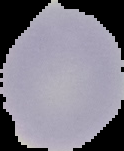

Summary:
  - Image size: 124×151 pixels
  - Image type: cell region segmented out of the field of view; surrounding area masked to black
  - Result: negative for Plasmodium parasites
  - Preparation: thin blood film